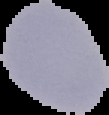
Summary:
  - Preparation: thin blood smear
  - Result: Plasmodium parasites identified
  - Image size: 109×115 pixels
  - Image type: segmented cell region with the area outside set to black